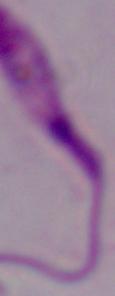
Micrograph. A Leishmania parasite is shown. Captured at 1000x magnification.